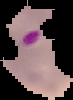

Summary:
  - Image size: 73×100 pixels
  - Image type: segmented cell region on a black background
  - Result: malaria parasites detected
  - Preparation: thin blood film